Classify this cell by malaria status.
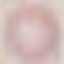

It is uninfected.

capture: smartphone camera at the microscope eyepiece
stain: Giemsa
preparation: thin smear
image_type: cell patch, automatically extracted from a larger field of view and resized to 64 × 64 pixels